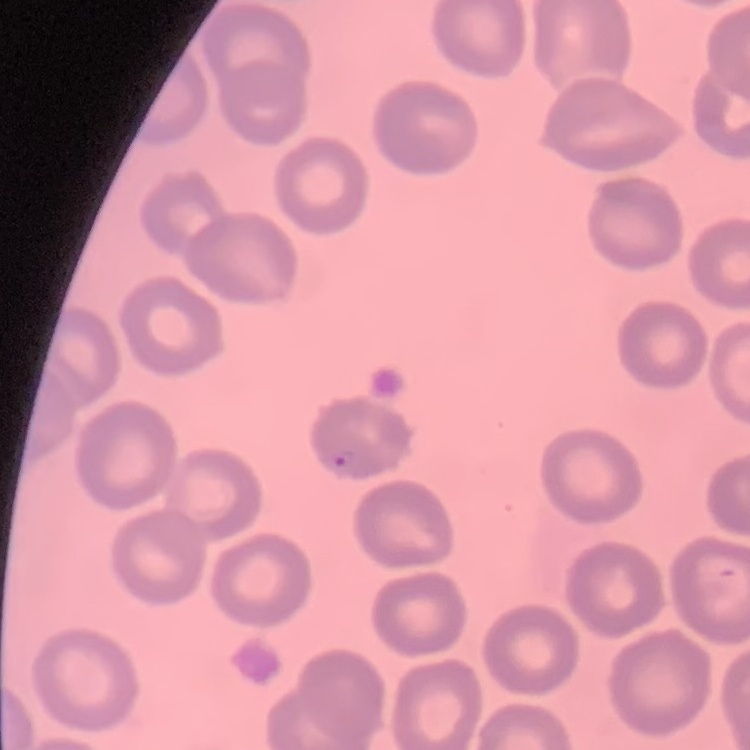

erythrocyte_morphology: no rouleaux formation
preparation: thin blood smear
image_type: square crop of a larger photomicrograph
stain: Field's or Giemsa